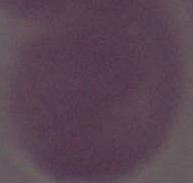

Summary:
  - Magnification: 1000x
  - Modality: photomicrograph
  - Identification: red blood cell